Classify this cell by malaria status.
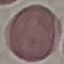
Uninfected.

Thin smear of blood. Giemsa stain. Photographed with a smartphone camera at the microscope eyepiece. Automatically extracted cell patch, resized to 64 × 64 pixels.